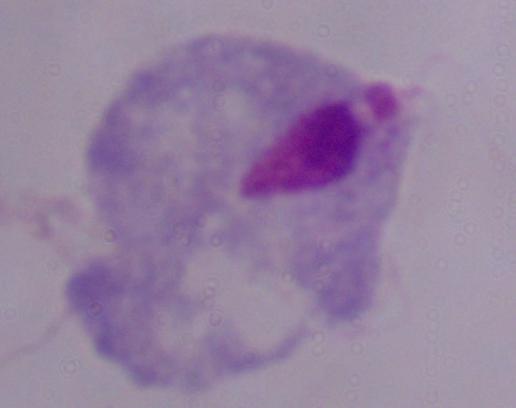

{
  "magnification": "1000x",
  "modality": "photomicrograph",
  "identification": "trichomonad"
}